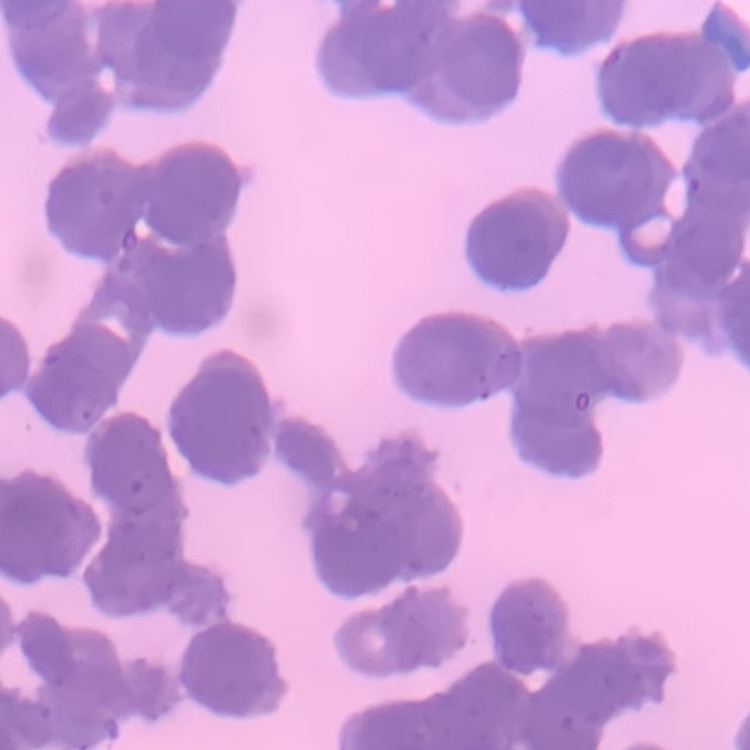
erythrocyte_morphology: rouleaux formation
stain: Field's or Giemsa
preparation: thin peripheral smear
image_type: square crop of a larger photomicrograph